Identify the parasite.
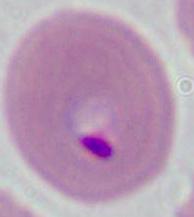

This is Plasmodium.

{
  "modality": "micrograph",
  "magnification": "400x or 1000x"
}